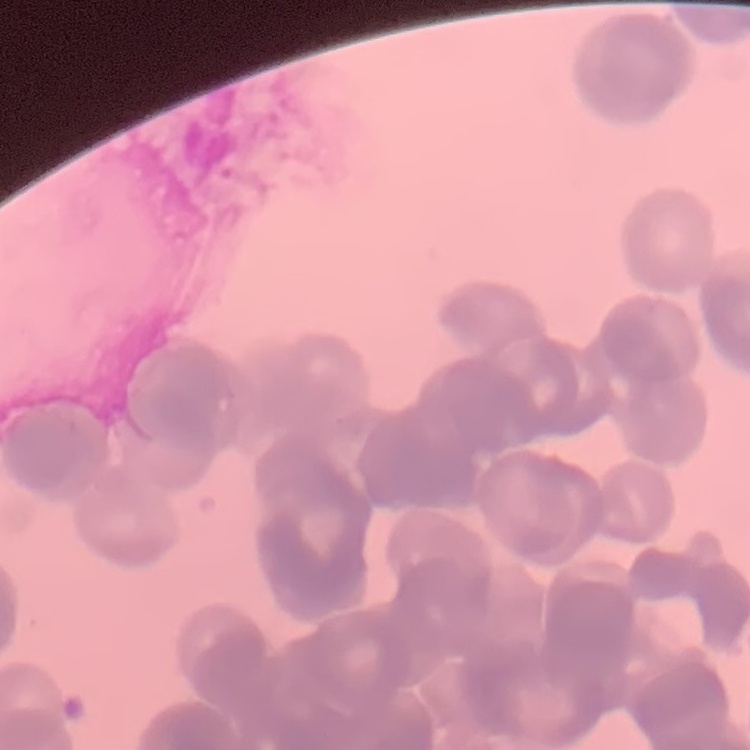
Summary:
  - Erythrocyte morphology: rouleaux formation
  - Preparation: thin blood film
  - Stain: Field's or Giemsa
  - Image type: square crop of a larger photomicrograph